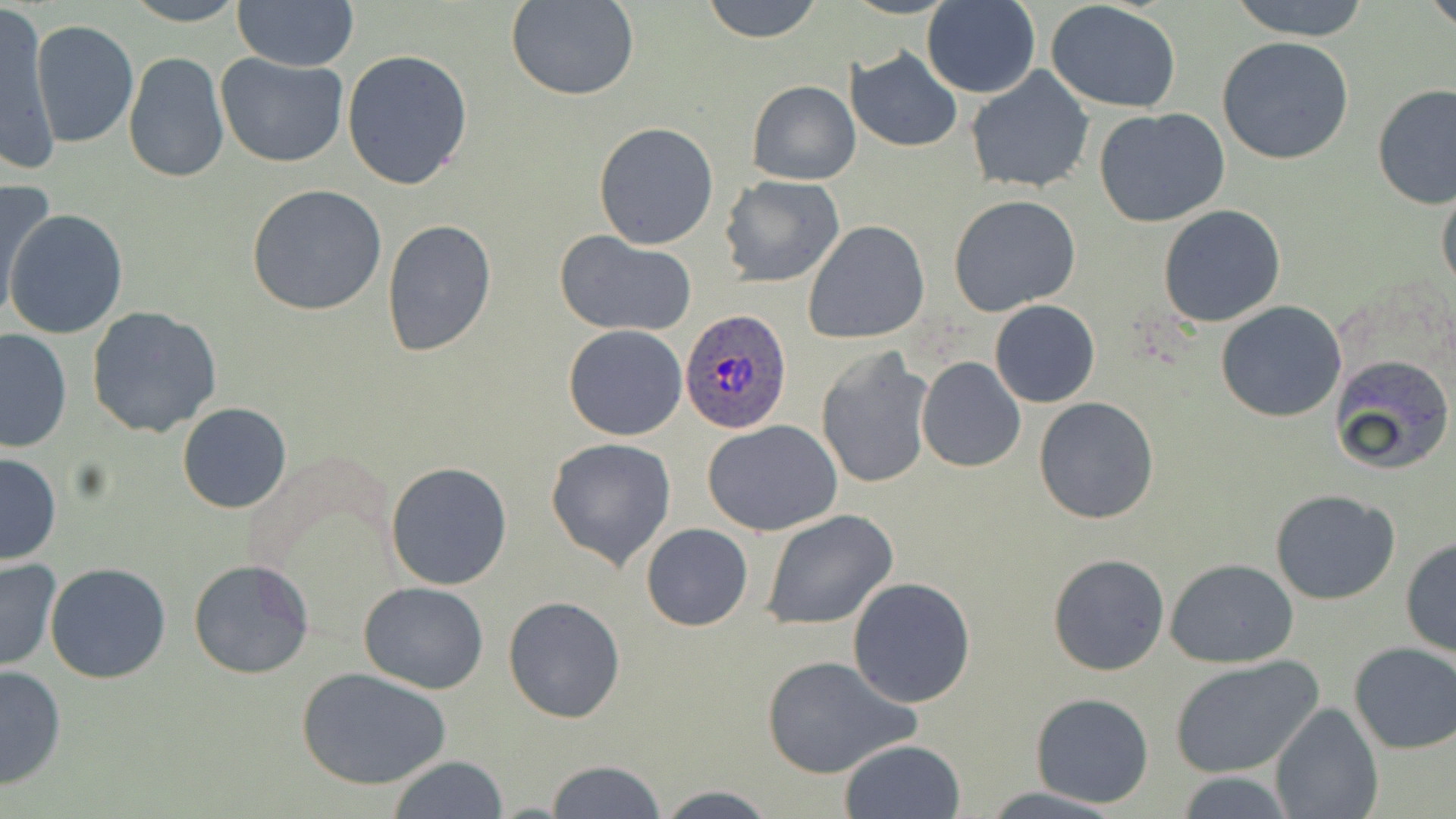 Approximate bounding boxes as [x1, y1, x2, y2] in pixels. Uninfected red blood cell locations: [122, 0, 247, 26], [231, 0, 360, 70], [505, 0, 641, 102], [701, 0, 824, 43], [921, 0, 1040, 97], [1225, 0, 1374, 41], [1425, 0, 1456, 34], [1046, 2, 1183, 112], [1, 7, 59, 173], [30, 20, 140, 150], [988, 31, 1137, 168], [1216, 37, 1356, 166], [845, 47, 963, 151], [342, 49, 474, 191], [122, 51, 229, 186], [216, 54, 349, 168], [965, 66, 1095, 194], [748, 80, 860, 185], [1372, 84, 1455, 209], [1094, 108, 1230, 228], [592, 121, 720, 251], [719, 175, 845, 287], [1436, 181, 1456, 298], [1, 183, 59, 326], [247, 185, 388, 316], [754, 186, 895, 322], [948, 195, 1082, 317], [1158, 204, 1286, 326], [5, 211, 129, 339], [383, 218, 496, 360], [803, 220, 930, 342], [555, 233, 697, 337], [989, 300, 1099, 408], [1215, 300, 1348, 422], [86, 306, 225, 439], [563, 324, 688, 441], [0, 330, 72, 452], [815, 348, 934, 490], [1328, 353, 1455, 474], [917, 357, 1025, 472], [729, 379, 906, 515], [1034, 396, 1160, 524], [176, 403, 292, 514], [702, 419, 846, 535], [545, 437, 677, 570], [0, 450, 61, 567], [387, 461, 512, 591], [1269, 489, 1400, 605], [761, 508, 898, 630], [641, 524, 752, 630], [1400, 539, 1456, 659], [1047, 553, 1171, 677], [0, 557, 62, 671], [1166, 559, 1299, 668], [187, 560, 314, 681], [44, 563, 172, 684], [847, 575, 977, 707], [358, 582, 489, 694], [503, 596, 628, 723], [1347, 643, 1456, 754], [759, 654, 920, 780], [1169, 656, 1323, 779], [0, 664, 66, 790], [299, 668, 451, 789], [1030, 693, 1155, 809], [1269, 701, 1383, 819], [839, 739, 966, 818], [387, 756, 511, 818], [545, 760, 667, 818], [1174, 771, 1296, 818], [654, 785, 776, 819], [982, 787, 1128, 818]. Plasmodium ovale-infected red blood cell locations: [680, 310, 793, 434]. Slide-level diagnosis: Plasmodium ovale. May-Grünwald-Giemsa stain. Optical microscopy. Thin blood smear. Image is 1456×819 pixels. Captured at 1000x magnification. Single field of view.